Comment on the morphology of the red blood cells.
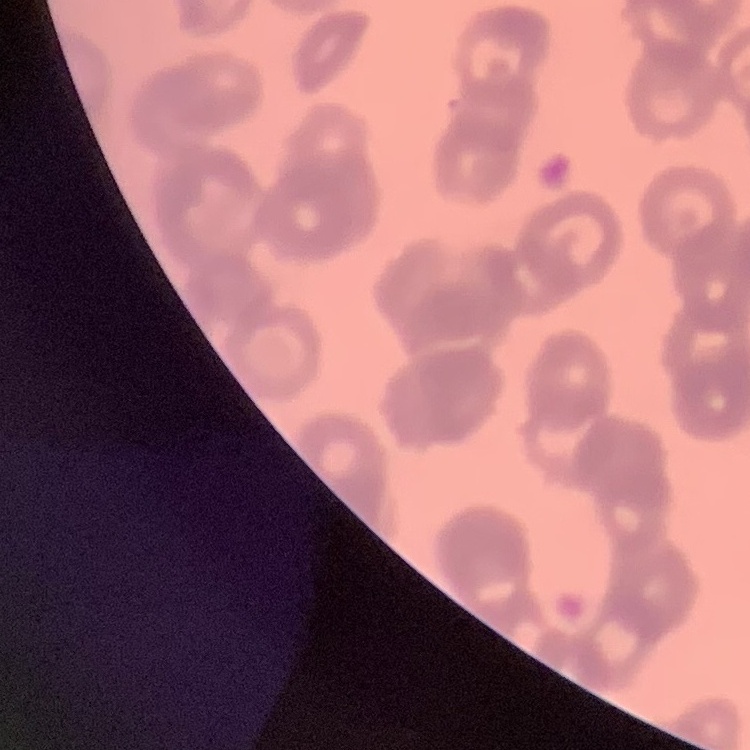
They show rouleaux formation.

Stained with either Field's or Giemsa. Square crop of a larger photomicrograph. Thin blood smear.